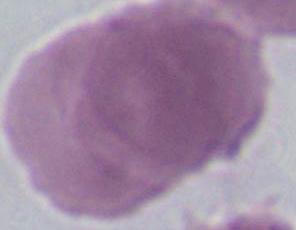 1000x magnification. Photomicrograph. An erythrocyte is shown.